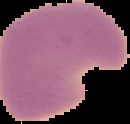 Result: malaria parasites identified. Cell region segmented out of the field of view; the surrounding area is masked to black. Image is 130×124 pixels. From a thin blood film.